Assess this cell for malaria.
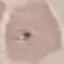
It is parasitized.

capture: smartphone camera at the microscope eyepiece
image_type: cell patch, automatically extracted from a larger field of view and resized to 64 × 64 pixels
preparation: thin blood film
stain: Giemsa